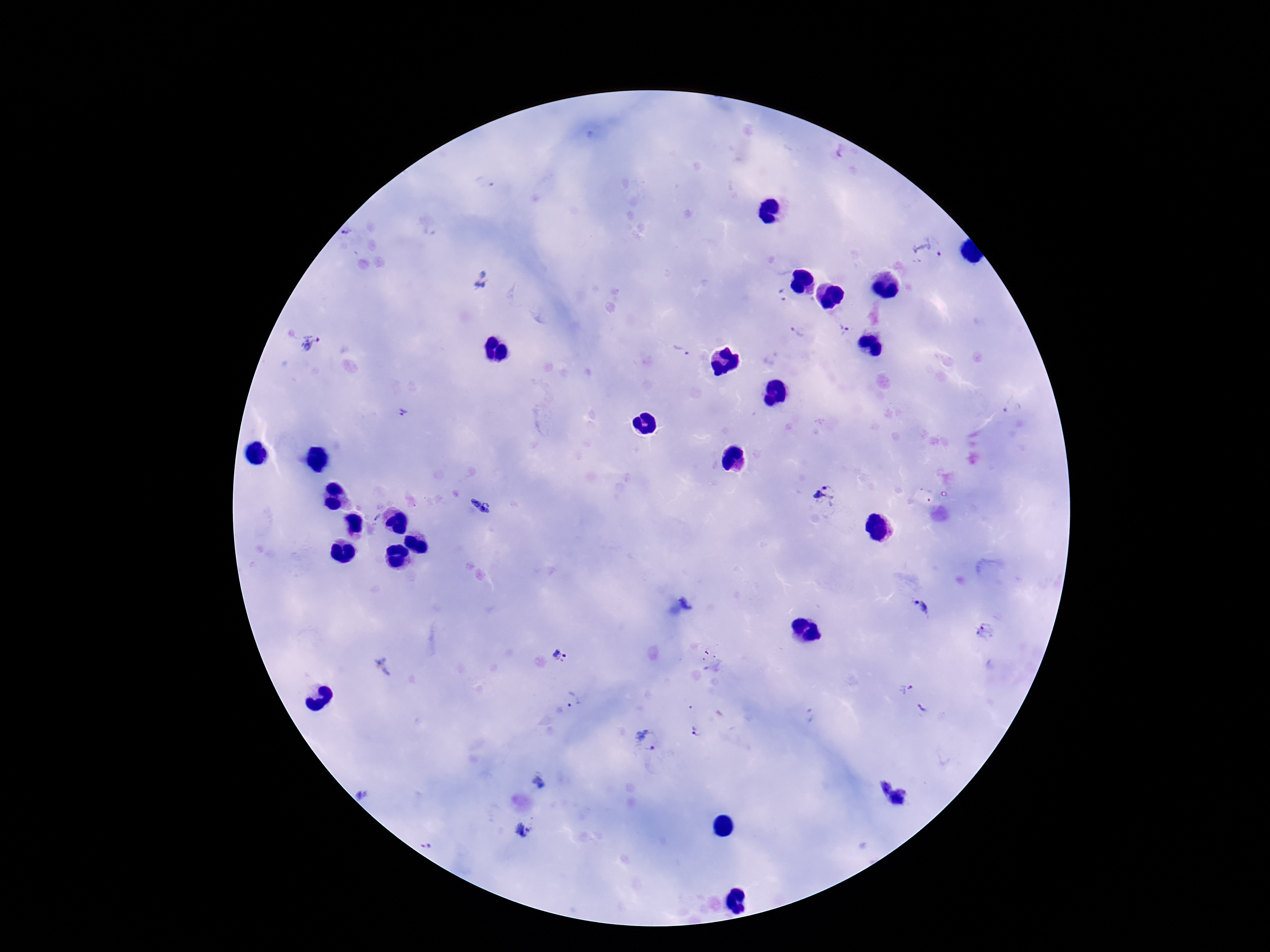

Approximate centers as [x, y] in pixels. Plasmodium parasite locations: [842, 154], [929, 247], [482, 280], [781, 297], [844, 329], [798, 332], [310, 344], [679, 353], [1014, 407], [403, 412], [824, 497], [482, 507], [376, 518], [923, 609], [985, 630], [560, 654], [384, 666], [904, 690], [574, 701], [923, 709], [808, 715], [695, 731], [648, 740], [539, 780], [893, 794], [363, 796], [524, 832], [429, 845]. Thick peripheral-blood smear. Patient malaria status: infected. One field from this slide. Image is 1270×952 pixels. Giemsa stain. Photographed through the microscope eyepiece with a smartphone camera. 100x magnification.